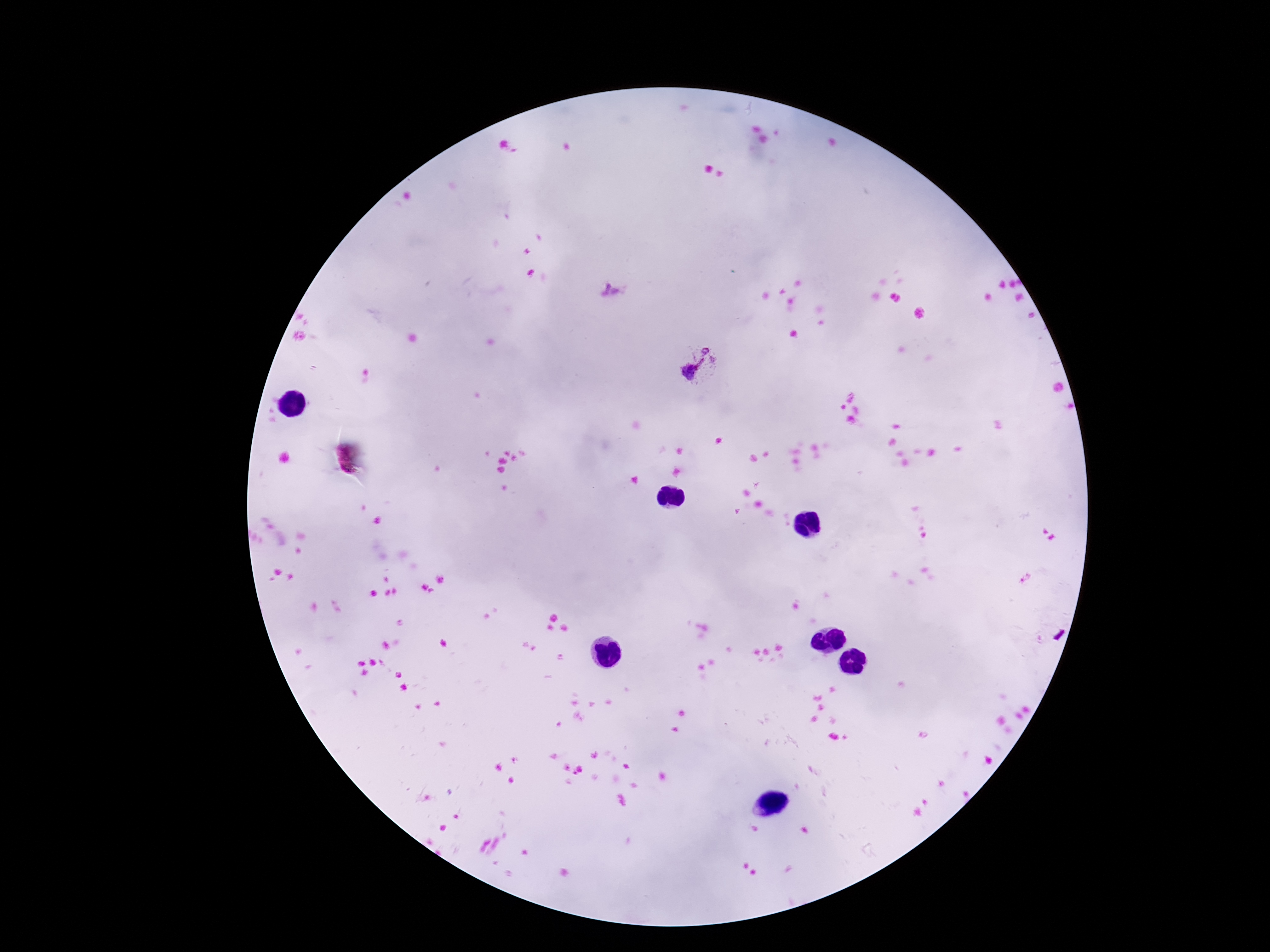
field of view = one from this slide
magnification = 100x
image size = 1270×952 pixels
preparation = thick blood film
stain = Giemsa
Plasmodium parasite locations = approximate centers as (x, y) in pixels: (612, 290), (698, 367)
capture = smartphone camera through the microscope eyepiece
patient malaria status = infected